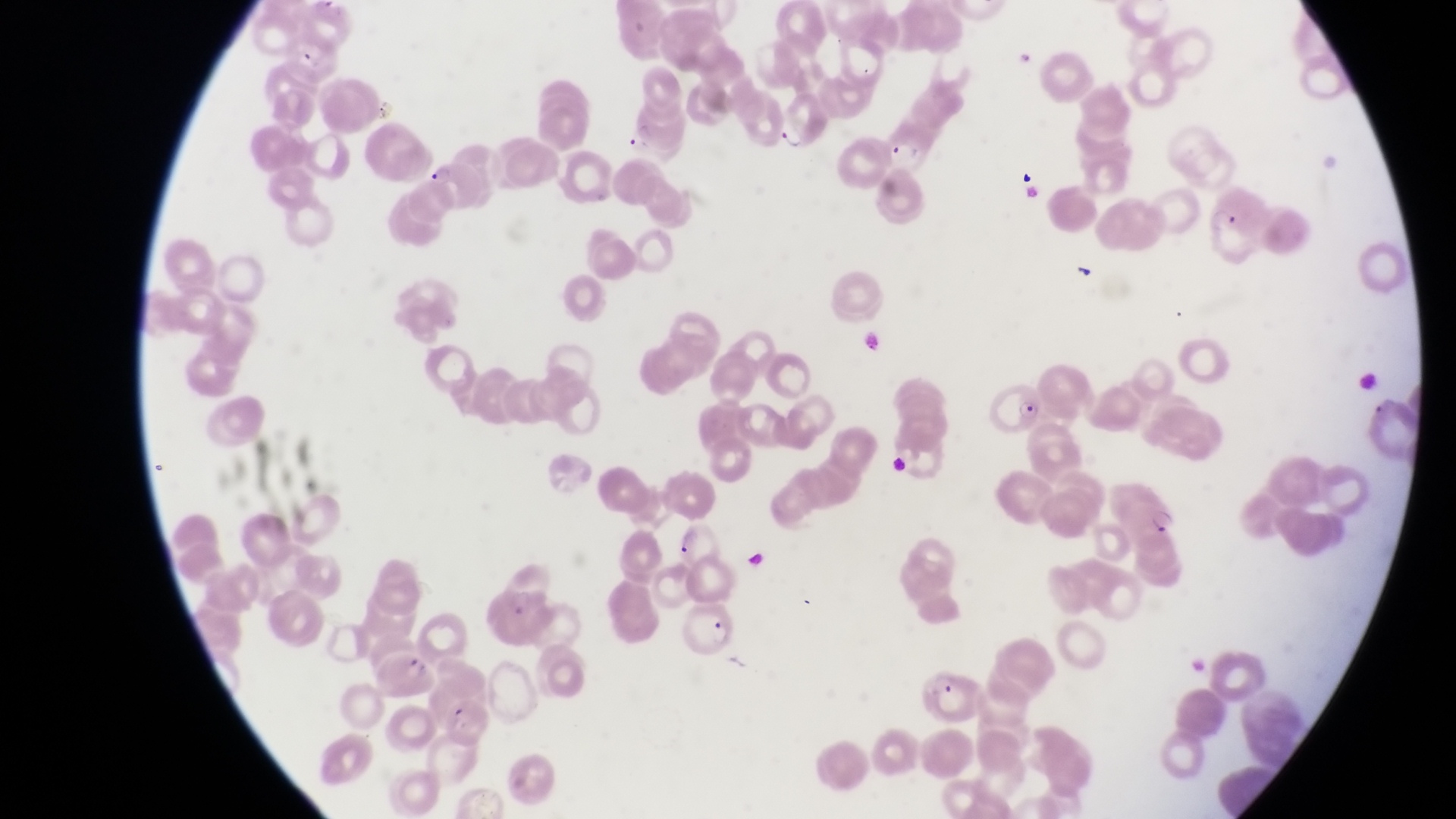 Approximate bounding boxes as (left, top, right, bottom) in pixels. Parasitised red blood cell locations: (880, 127, 926, 175), (425, 161, 484, 213), (988, 370, 1049, 444), (682, 607, 745, 662), (376, 642, 437, 703), (922, 666, 983, 725). Trophozoite locations: (774, 116, 801, 153), (1207, 199, 1244, 238), (1366, 381, 1399, 420), (1150, 505, 1182, 538). Artifact (platelet-like body, stain precipitate, or debris) locations: (1070, 258, 1104, 288). At a magnification of 1000x. Photographed through the eyepiece of an Olympus CX-23 microscope with a smartphone camera. Collected in Uganda. Single field of view. Image is 1456×819 pixels. Thin blood film.